Classify this cell by malaria status.
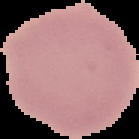

Uninfected.

From a thin blood film. The area outside the segmented cell region is set to black. Image is 139×139 pixels.